Describe the morphology of the red blood cells.
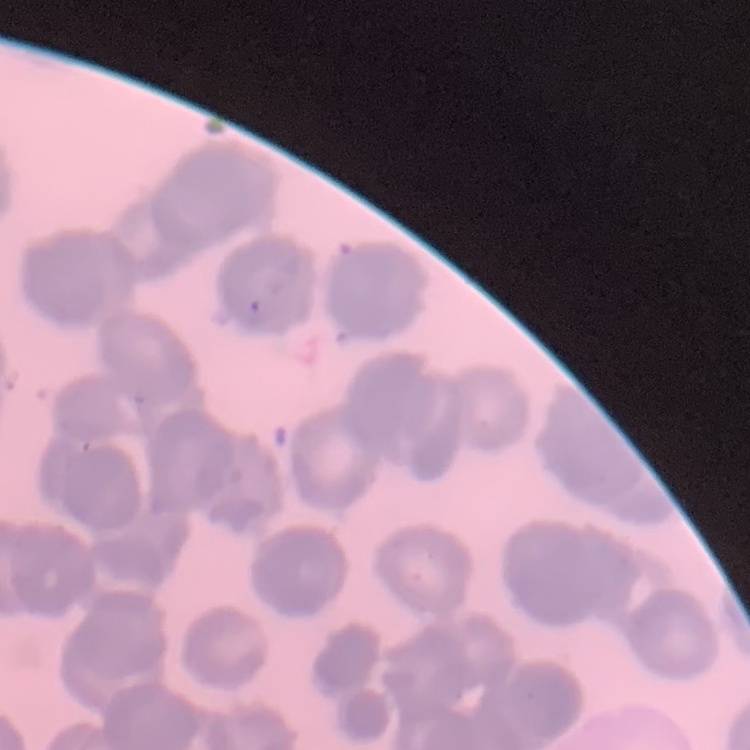
They show rouleaux formation.

Summary:
  - Stain: Field's or Giemsa
  - Image type: one tile cut from a larger photomicrograph
  - Preparation: thin blood film